Report the malaria status.
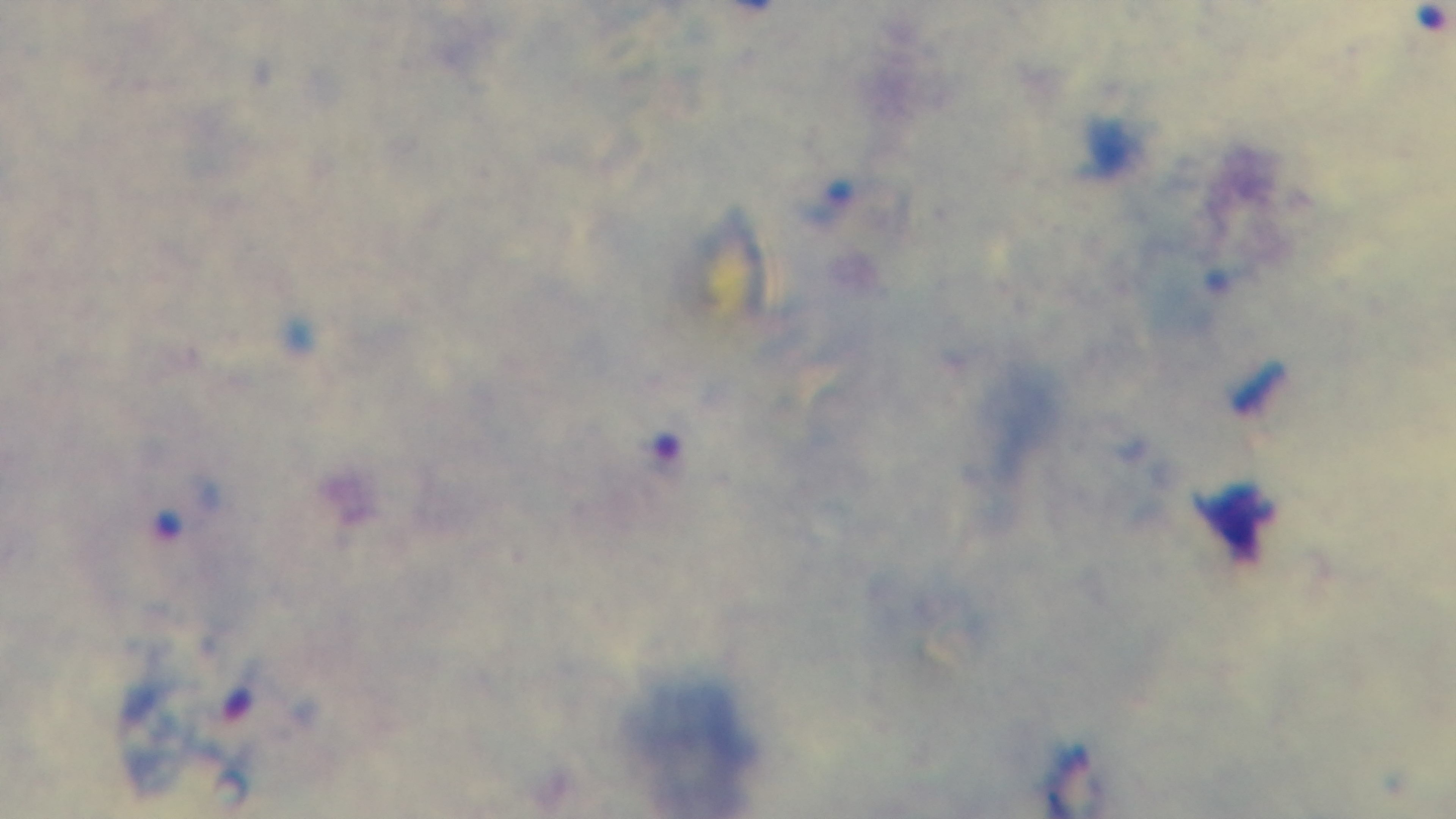
It is infected.

Summary:
  - Field of view: one from the slide
  - Modality: light microscopy
  - Capture: mounted 4K digital camera
  - Stain: Giemsa
  - Preparation: thick blood film
  - Objective: 100x oil immersion